Assess this cell for malaria.
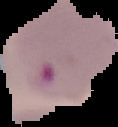
Parasitized.

The area outside the segmented cell region is set to black. From a thin blood smear. Image is 118×127 pixels.